Name the parasite shown.
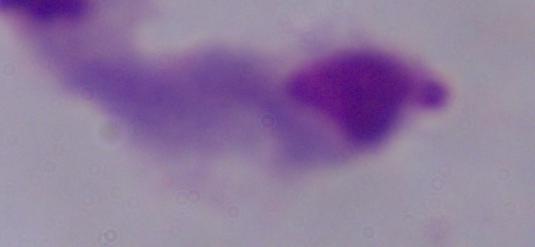

A trichomonad.

Summary:
  - Magnification: 1000x
  - Modality: micrograph